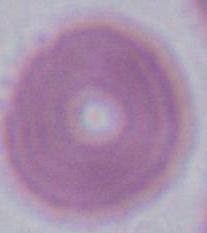
Summary:
  - Identification: erythrocyte
  - Modality: micrograph
  - Magnification: 1000x